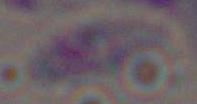
Summary:
  - Magnification: 1000x
  - Identification: Toxoplasma gondii
  - Modality: photomicrograph